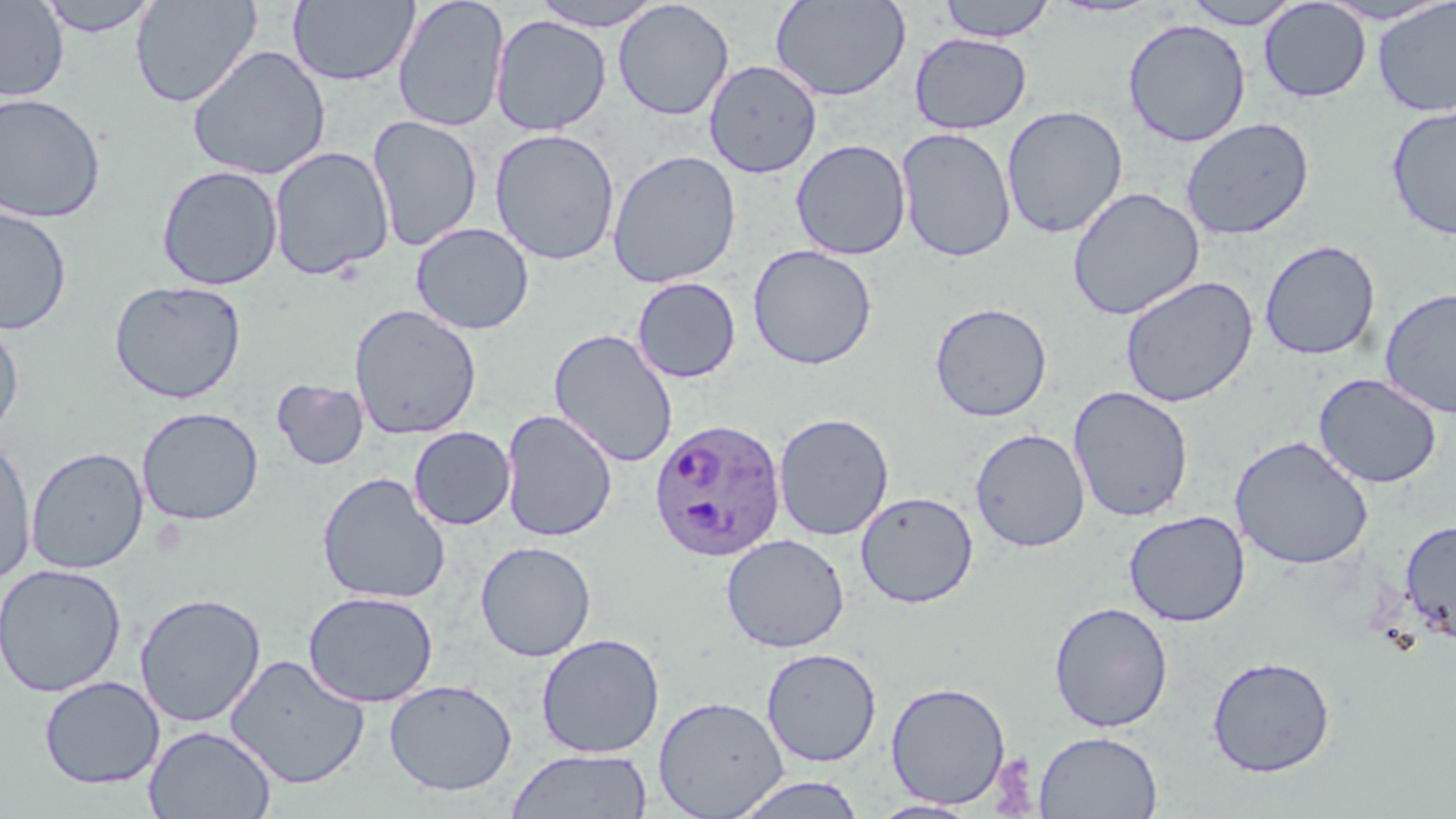
Approximate bounding boxes as [x1, y1, x2, y2] in pixels. Plasmodium ovale-infected red blood cell locations: [649, 418, 787, 562]. Uninfected red blood cell locations: [36, 0, 161, 37], [130, 0, 261, 108], [392, 0, 511, 133], [529, 0, 667, 31], [770, 0, 911, 101], [937, 0, 1056, 42], [1049, 0, 1165, 18], [1182, 0, 1304, 29], [0, 1, 69, 103], [287, 1, 420, 87], [613, 1, 735, 121], [1259, 1, 1371, 102], [1372, 1, 1456, 117], [491, 15, 612, 136], [1122, 18, 1251, 147], [909, 33, 1033, 134], [187, 45, 332, 180], [704, 59, 822, 177], [0, 92, 106, 223], [1001, 104, 1128, 239], [1385, 105, 1456, 240], [367, 115, 484, 252], [1180, 117, 1315, 241], [896, 127, 1017, 262], [489, 128, 621, 266], [791, 139, 911, 260], [268, 146, 394, 280], [607, 150, 742, 289], [156, 165, 283, 290], [1067, 187, 1205, 321], [0, 206, 72, 335], [411, 222, 534, 335], [1260, 240, 1381, 360], [747, 244, 878, 370], [1120, 275, 1258, 408], [631, 277, 742, 383], [109, 279, 247, 404], [1379, 287, 1456, 418], [929, 302, 1053, 422], [349, 304, 482, 440], [0, 316, 25, 441], [548, 328, 679, 468], [1313, 372, 1443, 489], [271, 379, 369, 470], [1067, 385, 1195, 522], [136, 406, 264, 526], [500, 409, 618, 542], [773, 412, 894, 541], [408, 426, 515, 530], [970, 427, 1091, 553], [1230, 435, 1374, 569], [0, 438, 36, 584], [27, 446, 148, 574], [316, 471, 451, 604], [855, 491, 979, 608], [1124, 510, 1250, 627], [1399, 520, 1456, 643], [721, 534, 850, 653], [475, 540, 597, 662], [0, 563, 127, 697], [302, 590, 439, 707], [134, 592, 267, 727], [1049, 602, 1173, 732], [535, 632, 665, 758], [761, 647, 882, 767], [225, 654, 370, 789], [1207, 655, 1336, 777], [39, 675, 165, 789], [384, 679, 517, 796], [885, 680, 1012, 809], [653, 695, 789, 818], [144, 724, 276, 819], [1034, 730, 1163, 818], [506, 748, 652, 819], [729, 775, 867, 818], [867, 799, 982, 818]. Slide-level diagnosis: Plasmodium ovale. May-Grünwald-Giemsa-stained preparation. One field of a larger specimen. Thin blood smear. Optical microscopy. Image is 1456×819 pixels. Captured at 1000x magnification.